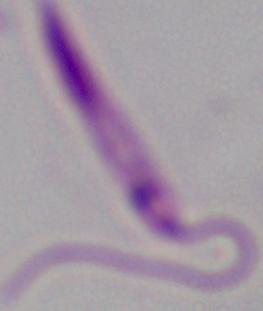
Summary:
  - Identification: Leishmania
  - Magnification: 1000x
  - Modality: micrograph